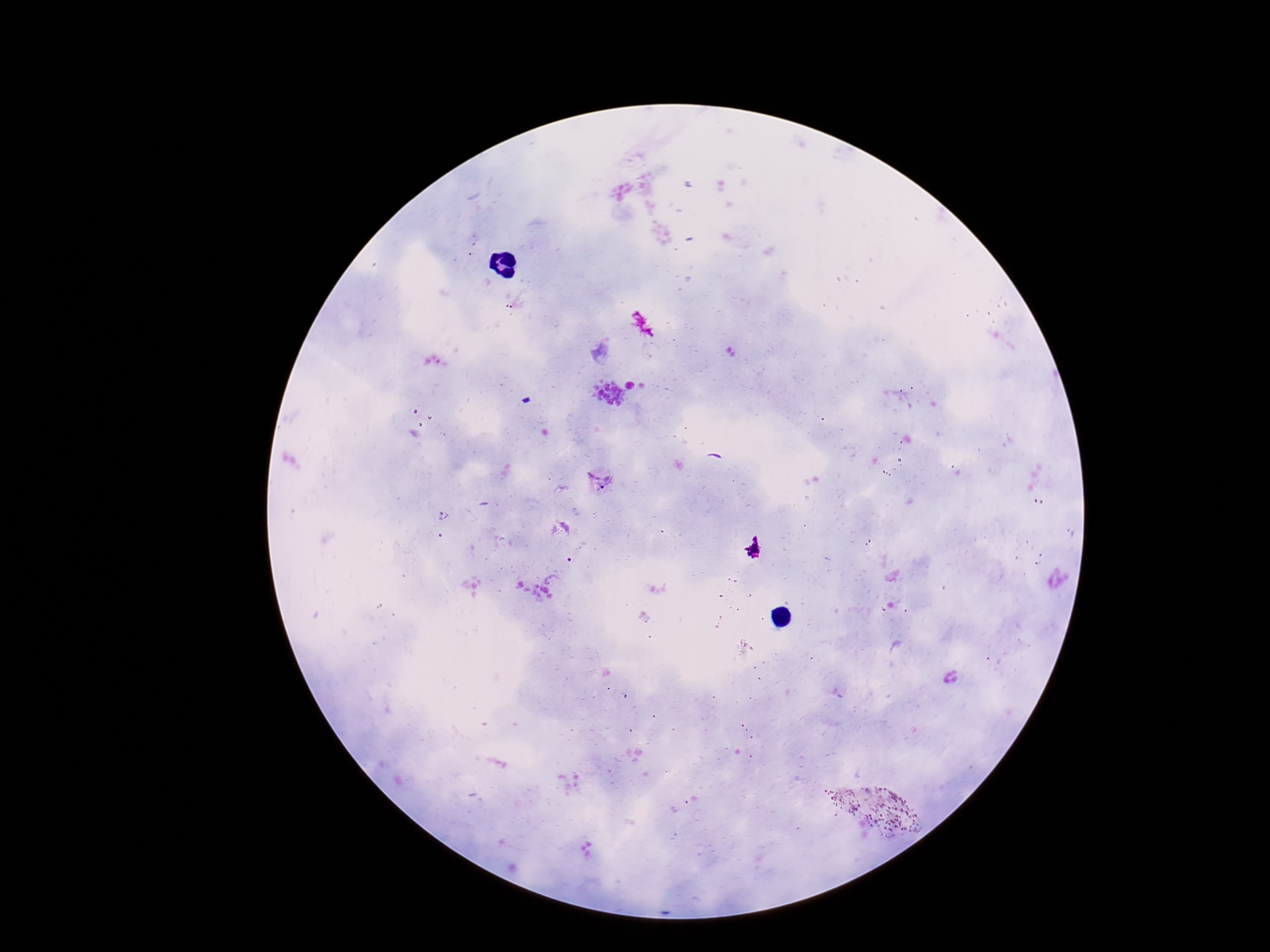
{
  "stain": "Giemsa",
  "plasmodium_parasite_locations": "approximate centers as [x, y] in pixels: [600, 479]",
  "magnification": "100x",
  "patient_malaria_status": "infected",
  "preparation": "thick blood film",
  "image_size": "1270×952 pixels",
  "field_of_view": "one from this slide",
  "capture": "smartphone camera through the microscope eyepiece"
}